Assess this cell for malaria.
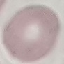

It is uninfected.

Giemsa stain. Thin smear of blood. Acquired by smartphone through the microscope eyepiece. Automatically extracted cell patch, resized to 64 × 64 pixels.